Give the position of every leukocyte visible.
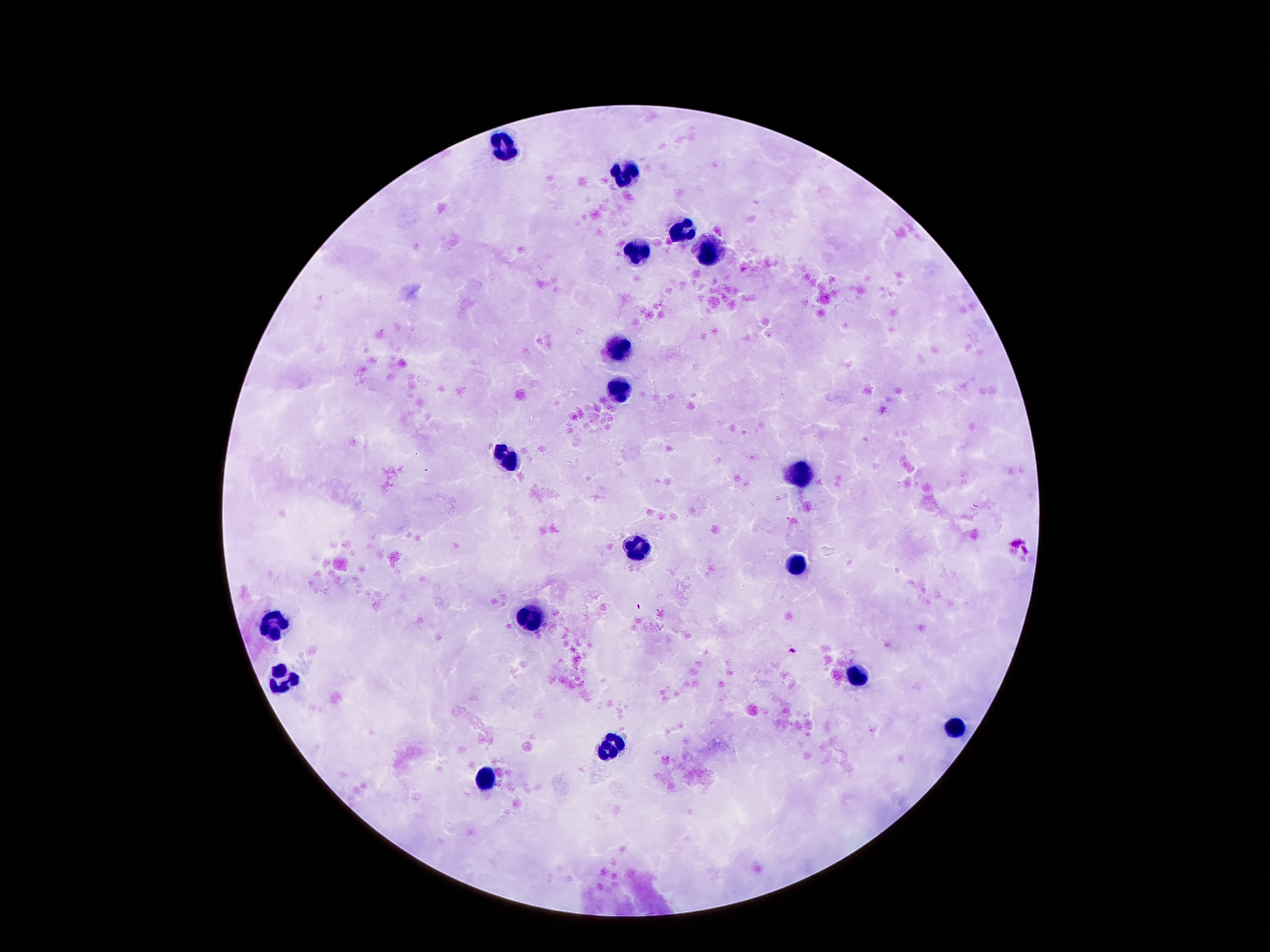
Approximate centers as [x, y] in pixels.
Leukocytes: [505, 144], [624, 174], [682, 231], [710, 249], [638, 251], [621, 349], [620, 393], [508, 459], [802, 474], [640, 551], [799, 569], [529, 617], [277, 620], [856, 678], [282, 680], [956, 728], [611, 746], [488, 780].

Photographed through the microscope eyepiece with a smartphone camera. Giemsa-stained preparation. Thick blood smear. 100x magnification. Image is 1270×952 pixels. One field from this slide. Patient malaria status: uninfected.